Name the parasite shown.
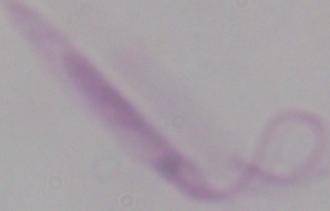

Leishmania.

Captured at 1000x magnification. Photomicrograph.